Assess this cell for malaria.
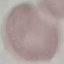
Uninfected.

stain = Giemsa
preparation = thin smear
image type = automatically extracted cell patch, resized to 64 × 64 pixels
capture = smartphone camera at the microscope eyepiece